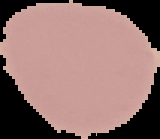

Image is 160×139 pixels. Malaria status: uninfected. The area outside the segmented cell region is set to black. From a thin blood film.